State which cell type is depicted.
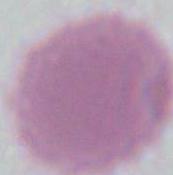

This is an erythrocyte.

Summary:
  - Magnification: 1000x
  - Modality: micrograph